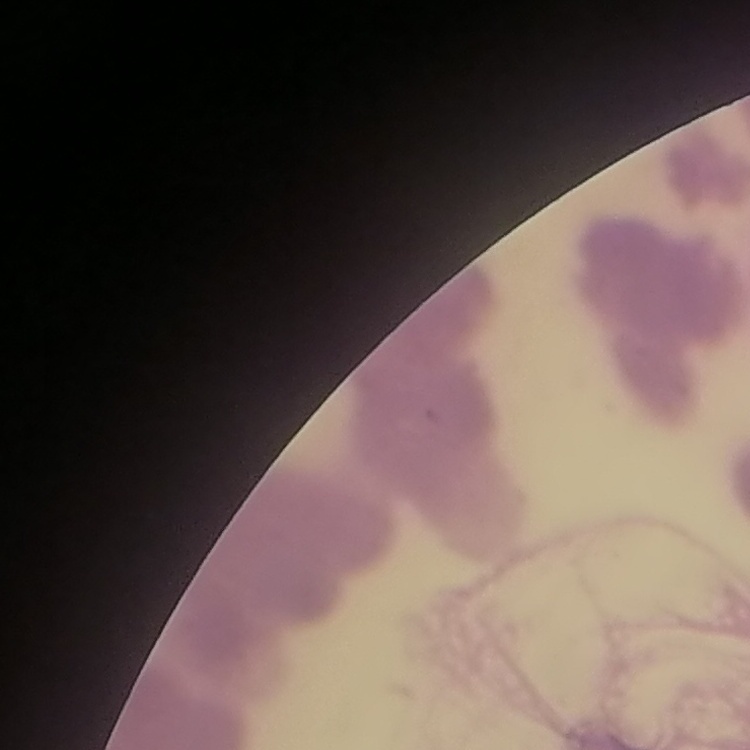

erythrocyte morphology = rouleaux formation
stain = Field's or Giemsa
image type = square crop of a larger photomicrograph
preparation = thin blood film